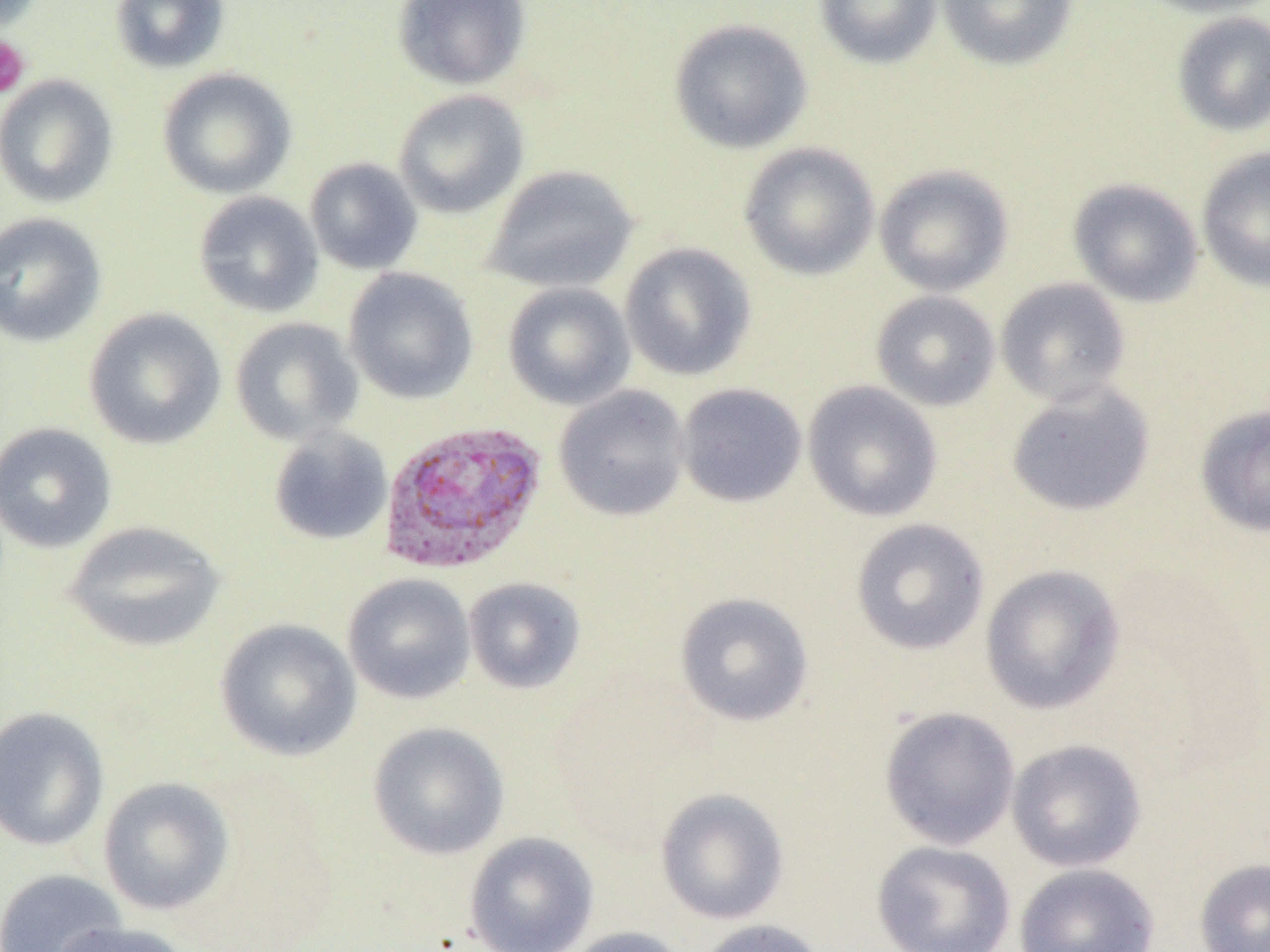

Summary:
  - Coordinate format: approximate bounding boxes as (x1, y1, x2, y2) in pixels
  - Platelet locations: (0, 35, 31, 99)
  - Uninfected red blood cell locations: (110, 0, 230, 74), (393, 0, 532, 91), (813, 0, 943, 69), (937, 0, 1079, 72), (1134, 0, 1270, 18), (1171, 11, 1270, 137), (668, 17, 814, 154), (157, 68, 297, 199), (0, 75, 119, 208), (392, 89, 530, 219), (738, 142, 880, 280), (1196, 147, 1270, 293), (304, 158, 423, 275), (874, 164, 1014, 296), (483, 165, 639, 294), (1068, 178, 1204, 307), (193, 191, 324, 318), (0, 211, 107, 348), (619, 242, 757, 381), (343, 268, 479, 405), (995, 277, 1131, 406), (502, 281, 636, 410), (871, 291, 1000, 411), (83, 308, 227, 450), (230, 317, 364, 446), (802, 380, 943, 522), (675, 383, 807, 508), (1005, 383, 1156, 516), (553, 385, 691, 522), (1195, 404, 1270, 537), (0, 422, 117, 553), (267, 427, 393, 546), (850, 518, 990, 655), (63, 520, 225, 653), (980, 564, 1125, 715), (342, 573, 475, 704), (463, 576, 586, 694), (675, 591, 814, 727), (215, 618, 362, 761), (0, 706, 109, 851), (878, 707, 1020, 850), (368, 721, 510, 860), (1006, 738, 1147, 872), (98, 776, 235, 916), (655, 788, 790, 924), (463, 832, 599, 952), (871, 840, 1016, 952), (1194, 857, 1270, 952), (1013, 863, 1160, 952), (0, 868, 128, 952), (693, 919, 829, 952), (52, 920, 192, 952), (557, 926, 691, 952)
  - Plasmodium vivax-infected red blood cell locations: (377, 420, 548, 576)
  - Slide-level diagnosis: Plasmodium vivax
  - Image size: 1270×952 pixels
  - Field of view: one of a larger specimen
  - Modality: light microscopy
  - Preparation: thin blood smear
  - Magnification: 1000x